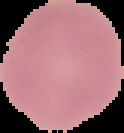
Summary:
  - Image size: 124×133 pixels
  - Malaria status: uninfected
  - Image type: cell region segmented out of the field of view; surrounding area masked to black
  - Preparation: thin blood smear